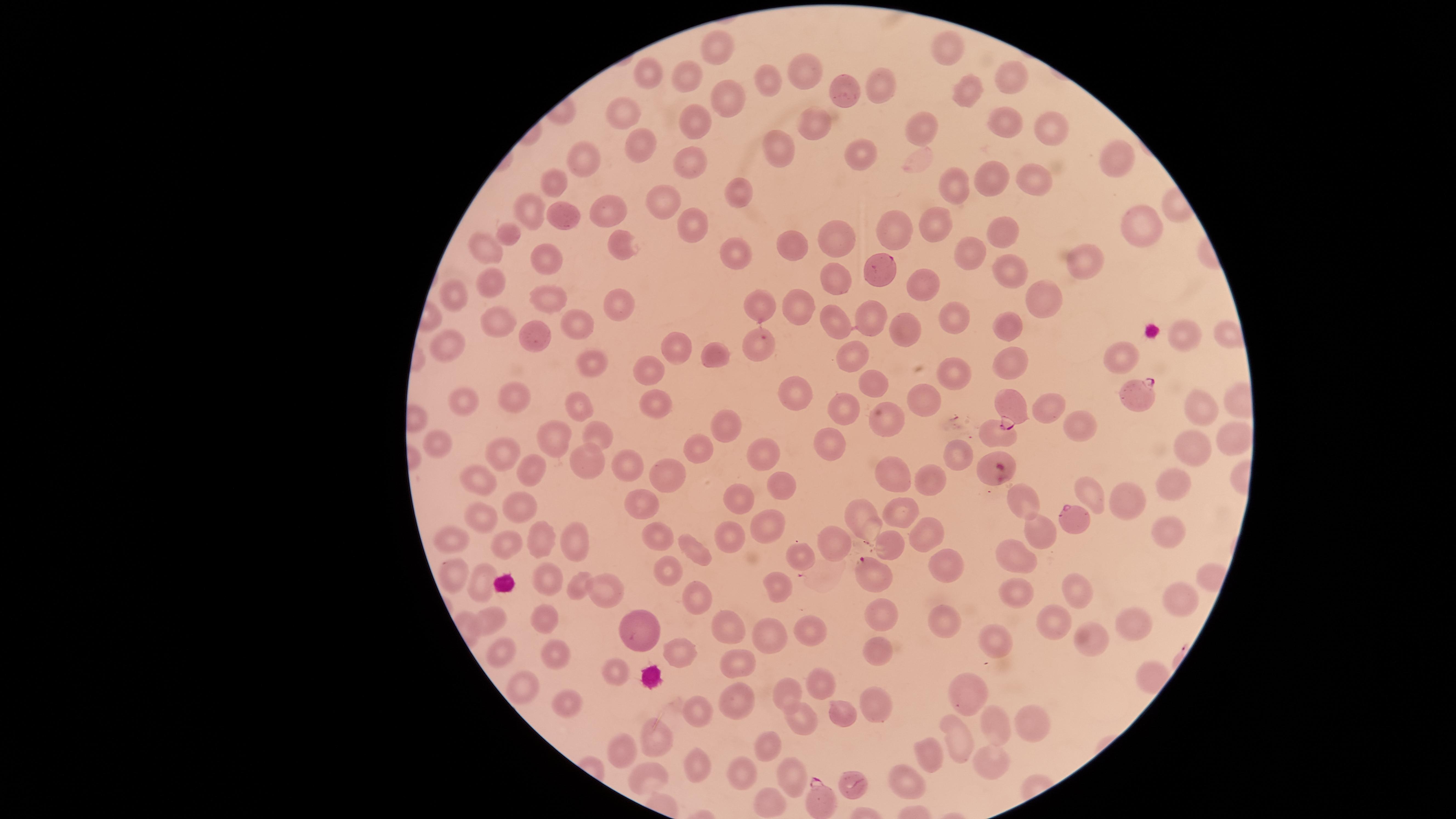
Approximate marker points as [x, y] in pixels.
Summary:
  - Parasitized red blood cells: [1141, 393], [1011, 403], [1073, 518], [876, 574], [854, 785], [821, 800]
  - Uninfected red blood cells: [714, 43], [944, 51], [806, 67], [647, 70], [687, 73], [1014, 80], [770, 81], [880, 85], [965, 93], [850, 95], [732, 106], [618, 110], [1005, 117], [698, 122], [819, 126], [1051, 128], [919, 130], [637, 144], [779, 145], [581, 152], [863, 159], [685, 160], [1111, 160], [990, 177], [555, 181], [1039, 181], [953, 188], [741, 196], [660, 203], [535, 207], [559, 210], [611, 213], [1136, 223], [935, 229], [507, 233], [693, 233], [899, 234], [618, 238], [1008, 239], [480, 245], [844, 247], [795, 248], [741, 252], [974, 256], [546, 264], [1094, 264], [1008, 269], [876, 270], [840, 283], [494, 284], [916, 285], [1047, 296], [454, 298], [555, 298], [615, 301], [764, 304], [803, 305], [867, 316], [953, 316], [499, 319], [579, 319], [902, 325], [1014, 326], [835, 327], [1179, 330], [543, 338], [758, 346], [450, 349], [847, 349], [674, 353], [713, 353], [1118, 356], [592, 360], [646, 365], [1010, 365], [955, 367], [791, 385], [869, 385], [920, 398], [465, 399], [506, 399], [659, 399], [584, 401], [1204, 405], [1043, 407], [843, 409], [887, 413], [1075, 422], [726, 424], [553, 433], [601, 436], [991, 437], [1231, 438], [830, 441], [443, 445], [699, 447], [510, 449], [953, 449], [761, 450], [1193, 450], [630, 464], [592, 465], [533, 470], [897, 471], [670, 472], [934, 477], [1181, 480], [483, 483], [781, 487], [1015, 491], [1085, 492], [735, 500], [641, 501], [1129, 502], [519, 508], [905, 508], [488, 514], [869, 518], [768, 524], [1042, 527], [1169, 527], [653, 530], [450, 534], [921, 534], [577, 537], [544, 538], [729, 538], [838, 539], [894, 543], [504, 545], [697, 552], [802, 555], [944, 560], [668, 562], [1019, 562], [451, 569], [478, 577], [545, 578], [579, 583], [777, 584], [607, 587], [1075, 589], [692, 595], [1184, 595], [1019, 597], [881, 612], [494, 619], [944, 620], [545, 622], [1056, 622], [637, 624], [1136, 627], [727, 628], [810, 629], [772, 630], [1092, 636], [994, 640], [678, 648], [501, 650], [877, 650], [548, 651], [743, 664], [616, 671], [820, 678], [525, 687], [789, 692], [967, 693], [562, 695], [737, 696], [871, 701], [696, 707], [845, 709], [799, 716], [996, 724], [1031, 724], [661, 735], [954, 743], [770, 744], [623, 745], [932, 756], [990, 760], [696, 764], [747, 769], [788, 771], [644, 774], [905, 786], [770, 803]
  - Field of view: single
  - Capture: smartphone photograph through the microscope eyepiece
  - Presence: malaria parasites seen
  - Stain: Giemsa
  - Preparation: thin blood film
  - Species: Plasmodium falciparum
  - Image size: 1456×819 pixels
  - Visible region: circular